Outline each Plasmodium malariae-infected red blood cell.
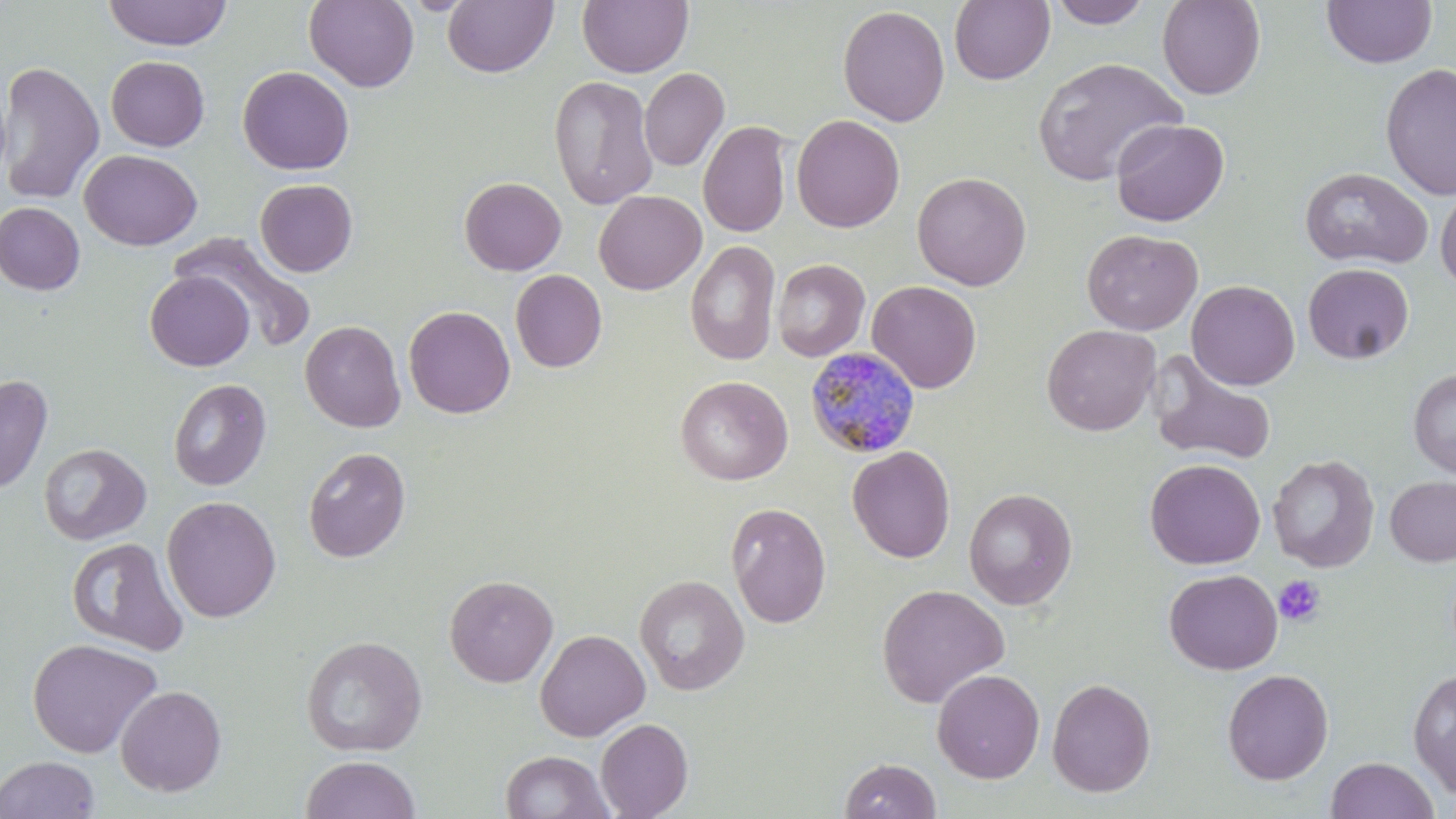
Approximate bounding boxes as (x1, y1, x2, y2) in pixels.
Plasmodium malariae-infected red blood cells: (804, 345, 921, 460).

slide-level diagnosis = Plasmodium malariae
magnification = 1000x
uninfected red blood cell locations = approximate bounding boxes as (x1, y1, x2, y2) in pixels: (101, 0, 233, 50), (304, 0, 419, 92), (443, 0, 557, 78), (577, 0, 693, 77), (949, 0, 1055, 85), (1047, 0, 1152, 28), (1157, 0, 1266, 100), (1321, 0, 1437, 69), (837, 5, 950, 127), (106, 55, 210, 151), (1032, 56, 1187, 186), (0, 60, 105, 205), (1380, 63, 1456, 201), (238, 66, 355, 175), (639, 67, 729, 172), (549, 75, 658, 210), (0, 78, 11, 185), (791, 114, 905, 233), (1110, 118, 1230, 226), (698, 120, 793, 238), (80, 149, 202, 250), (1298, 166, 1433, 270), (912, 171, 1031, 290), (459, 176, 566, 276), (254, 178, 358, 277), (1435, 187, 1456, 294), (594, 190, 707, 294), (1, 202, 85, 295), (1081, 228, 1203, 335), (171, 233, 318, 352), (686, 240, 780, 366), (772, 258, 869, 362), (1303, 263, 1414, 364), (510, 269, 607, 372), (145, 271, 254, 371), (866, 280, 982, 393), (1186, 280, 1300, 390), (403, 305, 516, 418), (300, 320, 405, 432), (1042, 324, 1161, 436), (1147, 353, 1277, 467), (1408, 368, 1456, 478), (0, 373, 53, 495), (675, 375, 793, 485), (168, 378, 271, 491), (39, 443, 151, 545), (303, 446, 412, 562), (847, 446, 956, 563), (1267, 455, 1379, 572), (1145, 459, 1266, 570), (1385, 475, 1456, 566), (963, 487, 1077, 609), (162, 495, 282, 623), (726, 502, 831, 628), (67, 537, 189, 657), (1164, 568, 1283, 675), (444, 574, 558, 687), (634, 574, 749, 695), (876, 584, 1010, 708), (535, 629, 650, 742), (300, 635, 427, 757), (26, 638, 162, 758), (931, 668, 1045, 783), (1222, 668, 1334, 784), (1408, 668, 1456, 798), (1047, 678, 1156, 797), (115, 684, 227, 796), (595, 718, 693, 818), (499, 750, 614, 819), (0, 755, 100, 818), (300, 755, 420, 819), (1325, 756, 1439, 819), (839, 758, 941, 819)
image size = 1456×819 pixels
preparation = thin blood smear
modality = light microscopy
stain = May-Grünwald-Giemsa
field of view = single
platelet locations = approximate bounding boxes as (x1, y1, x2, y2) in pixels: (1274, 575, 1326, 626)